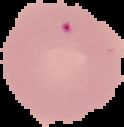 Image is 124×127 pixels. From a thin blood smear. Segmented cell region on a black background. Result: no Plasmodium parasites detected.